Locate every blood parasite and identify its species.
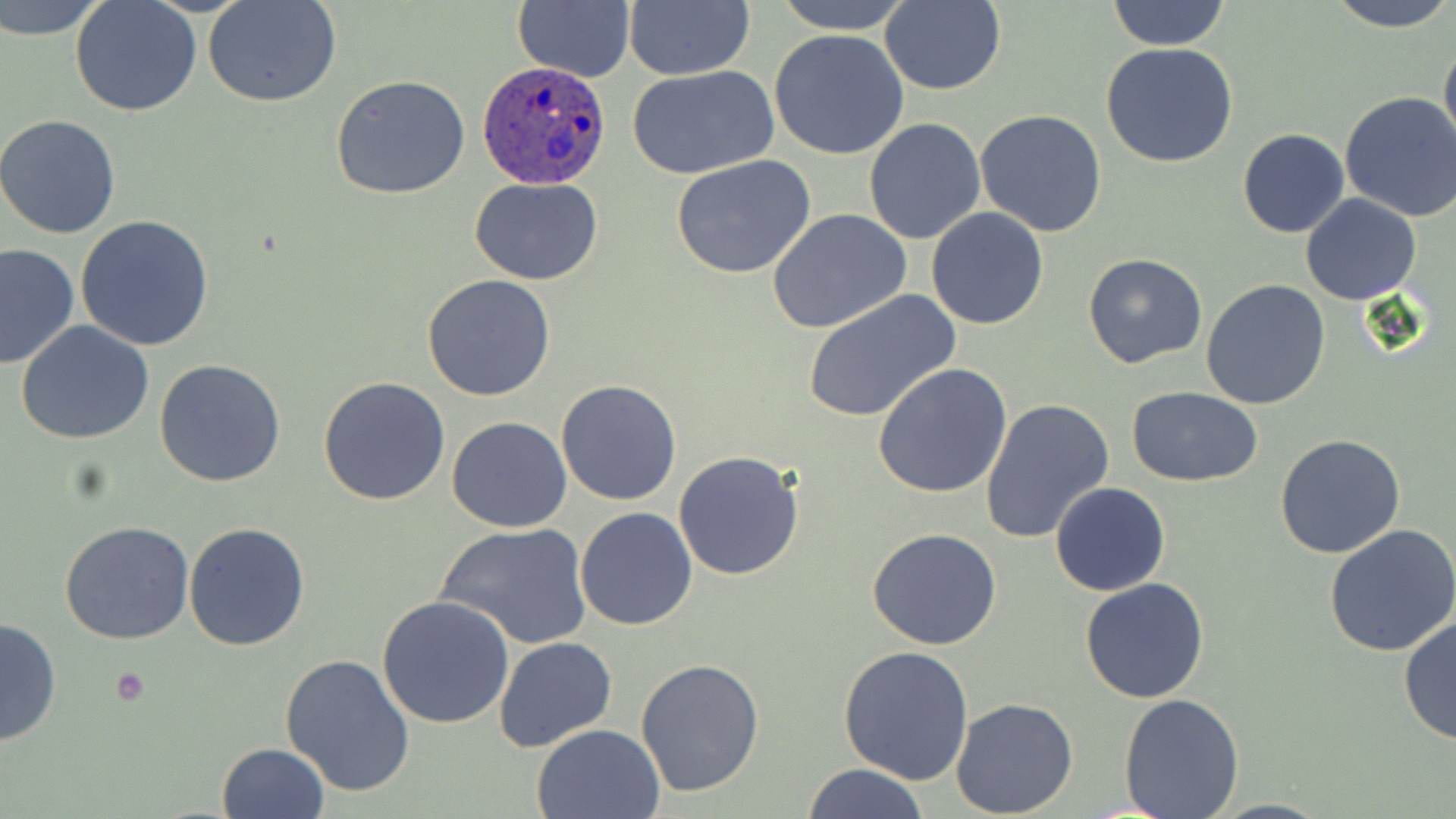

Approximate bounding boxes as [x1, y1, x2, y2] in pixels.
Plasmodium ovale-infected red blood cells: [477, 62, 615, 190].
No Plasmodium falciparum, Plasmodium malariae, Plasmodium vivax, Babesia divergens, or Trypanosoma brucei observed.

Uninfected red blood cell locations: [1, 0, 110, 39], [69, 0, 202, 117], [513, 0, 635, 83], [623, 0, 753, 82], [769, 0, 914, 35], [1107, 0, 1229, 51], [1325, 0, 1455, 33], [204, 1, 342, 108], [878, 1, 1006, 95], [769, 29, 912, 160], [1439, 35, 1456, 159], [1099, 43, 1239, 169], [626, 65, 778, 179], [330, 75, 471, 200], [640, 87, 801, 250], [1339, 90, 1456, 223], [975, 109, 1107, 237], [0, 115, 123, 239], [864, 117, 985, 245], [1237, 128, 1350, 239], [673, 157, 816, 280], [471, 178, 602, 286], [1300, 194, 1423, 305], [926, 207, 1050, 329], [768, 209, 914, 333], [74, 215, 215, 351], [0, 243, 79, 370], [1083, 253, 1209, 369], [422, 274, 555, 401], [1200, 280, 1331, 410], [802, 291, 959, 423], [15, 320, 154, 445], [155, 358, 287, 487], [874, 364, 1013, 500], [319, 375, 452, 505], [555, 380, 683, 506], [1126, 387, 1262, 487], [979, 397, 1115, 544], [446, 418, 572, 533], [1275, 433, 1406, 558], [673, 450, 805, 580], [1050, 481, 1170, 597], [574, 507, 699, 630], [61, 520, 195, 644], [184, 521, 309, 651], [435, 522, 593, 650], [1324, 522, 1456, 656], [867, 527, 1001, 650], [1080, 578, 1210, 703], [376, 593, 516, 728], [0, 614, 62, 749], [1398, 614, 1455, 745], [494, 636, 616, 751], [838, 643, 974, 785], [281, 653, 416, 797], [636, 657, 766, 797], [1118, 693, 1245, 818], [949, 698, 1078, 817], [531, 723, 665, 818], [216, 742, 330, 819], [801, 763, 930, 819], [1204, 798, 1335, 818]. Platelet locations: [112, 667, 151, 706]. Slide-level diagnosis: Plasmodium ovale. Light microscopy. May-Grünwald-Giemsa-stained preparation. 1000x magnification. Single field of view. Thin blood smear. Image is 1456×819 pixels.